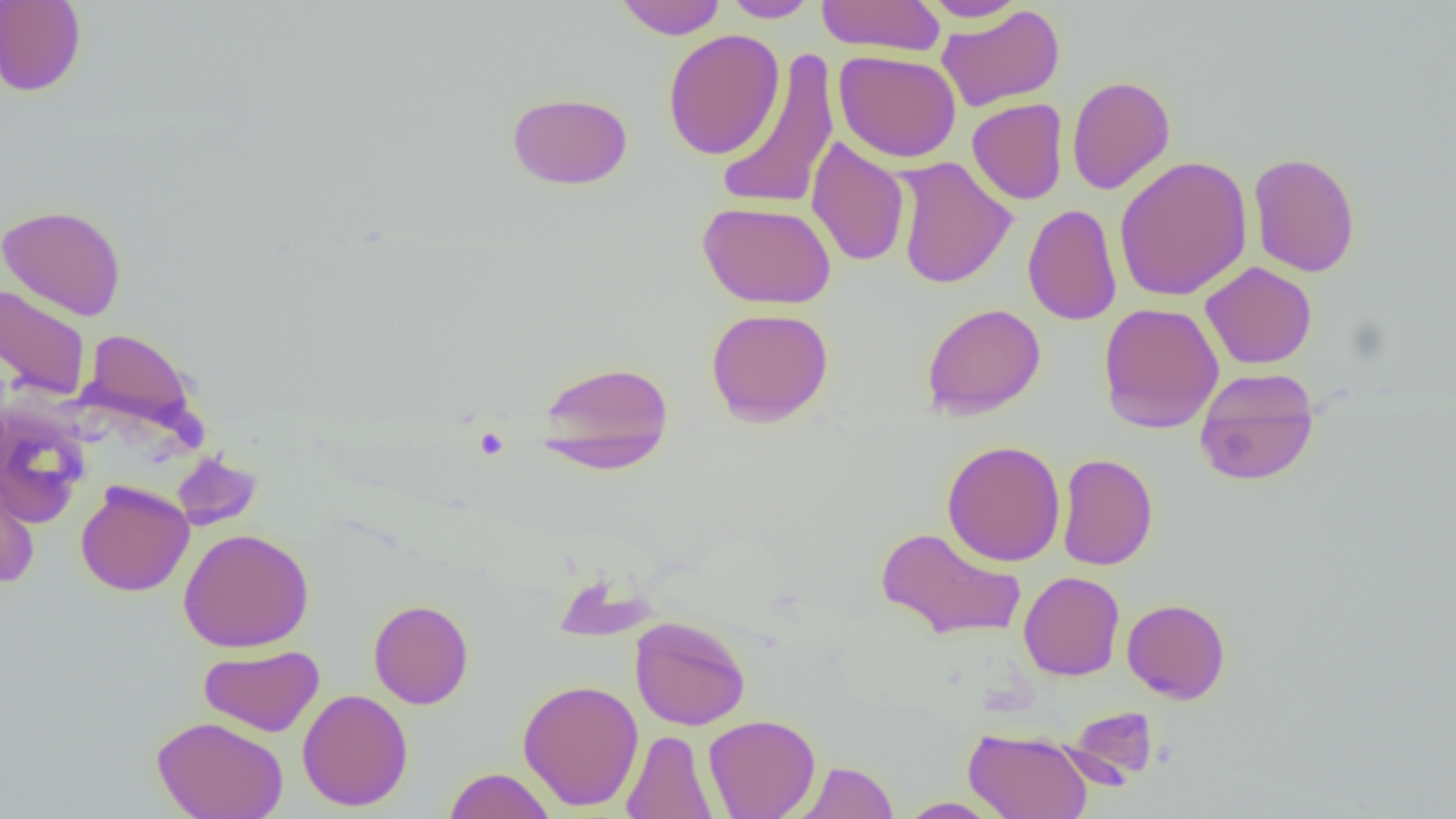
{
  "slide_level_diagnosis": "no evidence of blood parasites",
  "magnification": "1000x",
  "image_size": "1456×819 pixels",
  "field_of_view": "one of a larger specimen",
  "preparation": "thin blood smear",
  "modality": "light microscopy",
  "uninfected_red_blood_cell_locations": "approximate bounding boxes as (x1,y1)-(x2,y2) corner pairs in pixels: (0,0)-(87,97), (614,0)-(726,40), (721,0)-(820,22), (816,0)-(945,56), (918,0)-(1027,22), (936,4)-(1065,112), (662,29)-(784,160), (714,49)-(839,212), (833,50)-(961,163), (1067,75)-(1176,195), (506,91)-(633,190), (967,99)-(1068,205), (806,137)-(910,267), (1247,151)-(1361,278), (1113,155)-(1253,302), (893,156)-(1016,290), (697,200)-(837,309), (1023,203)-(1122,326), (0,204)-(126,320), (1201,261)-(1317,369), (0,284)-(91,400), (1097,302)-(1224,433), (922,303)-(1045,419), (705,307)-(834,427), (80,328)-(197,429), (537,360)-(674,472), (1194,368)-(1320,487), (0,407)-(91,527), (942,440)-(1066,566), (171,451)-(263,531), (1057,452)-(1158,570), (0,467)-(40,589), (75,479)-(194,596), (875,526)-(1027,642), (178,527)-(314,653), (1018,571)-(1124,681), (1122,598)-(1231,704), (368,599)-(474,709), (630,616)-(751,730), (198,645)-(324,737), (517,678)-(644,811), (297,688)-(413,811), (1062,705)-(1161,786), (703,714)-(820,819), (152,715)-(289,819), (964,728)-(1093,819), (622,729)-(718,819), (795,761)-(898,819), (444,767)-(556,819), (896,796)-(1006,818)"
}